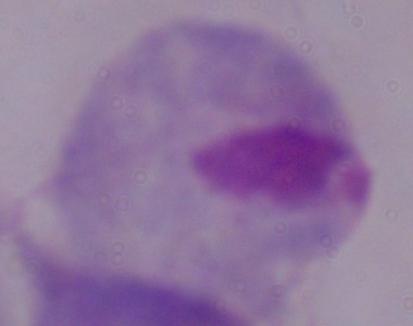
Summary:
  - Modality: micrograph
  - Identification: trichomonad
  - Magnification: 1000x